Point out each Plasmodium parasite.
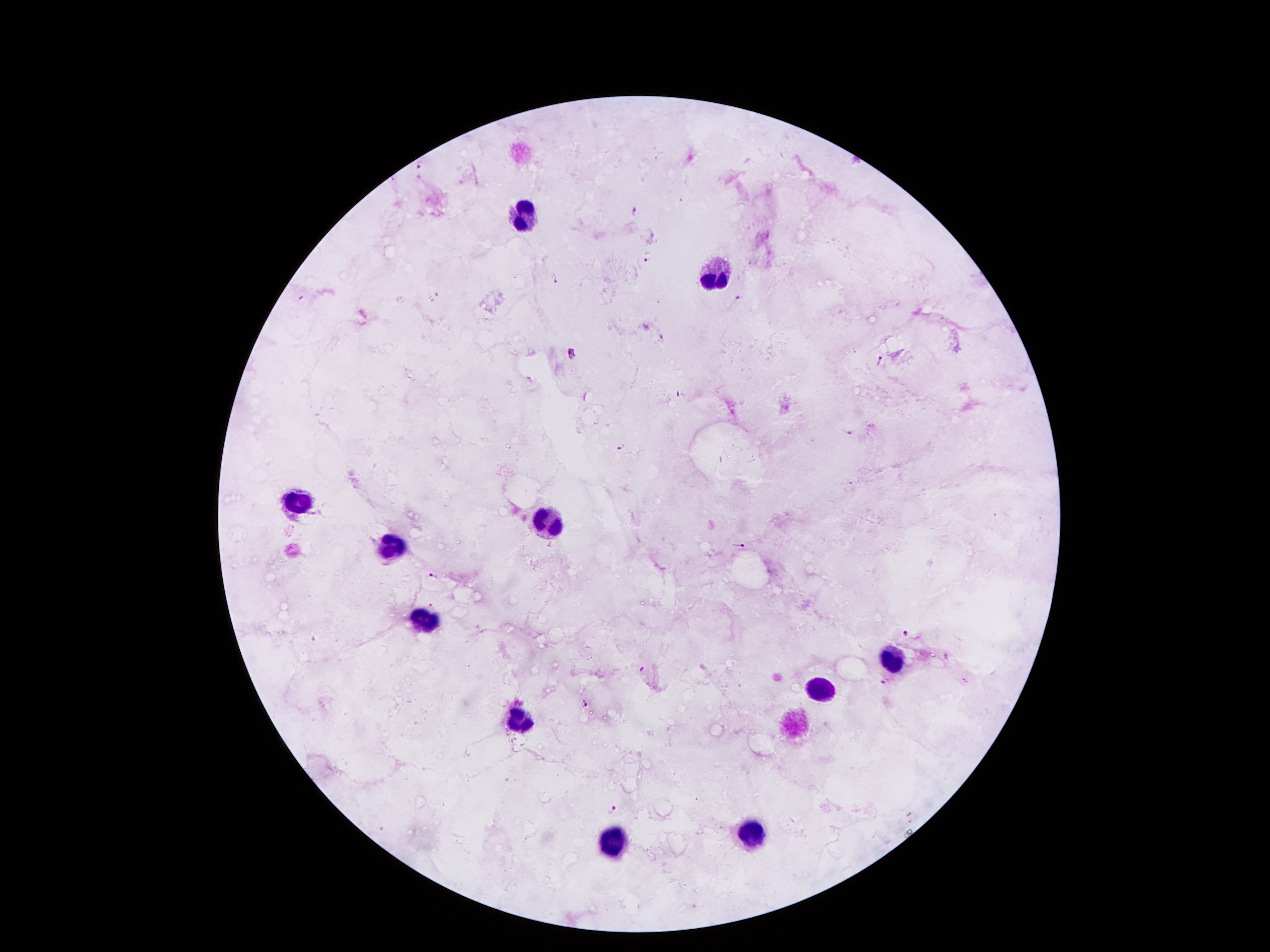

Approximate object centers, in pixels from the top-left corner.
Plasmodium parasites: (x=422, y=162), (x=634, y=209), (x=645, y=256), (x=557, y=279), (x=739, y=301), (x=662, y=337), (x=571, y=352), (x=880, y=361), (x=849, y=431), (x=623, y=446), (x=742, y=545), (x=434, y=576), (x=908, y=633), (x=644, y=669), (x=882, y=682), (x=586, y=701), (x=611, y=808).

Summary:
  - Leukocyte locations: (x=526, y=213), (x=716, y=274), (x=300, y=503), (x=551, y=526), (x=396, y=548), (x=421, y=622), (x=888, y=663), (x=823, y=690), (x=523, y=722), (x=743, y=839), (x=609, y=840)
  - Magnification: 100x
  - Stain: Giemsa
  - Patient malaria status: positive for Plasmodium falciparum
  - Capture: smartphone camera through the microscope eyepiece
  - Image size: 1270×952 pixels
  - Field of view: single
  - Preparation: thick peripheral-blood smear